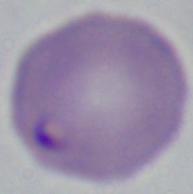
magnification = 1000x
identification = Babesia
modality = photomicrograph